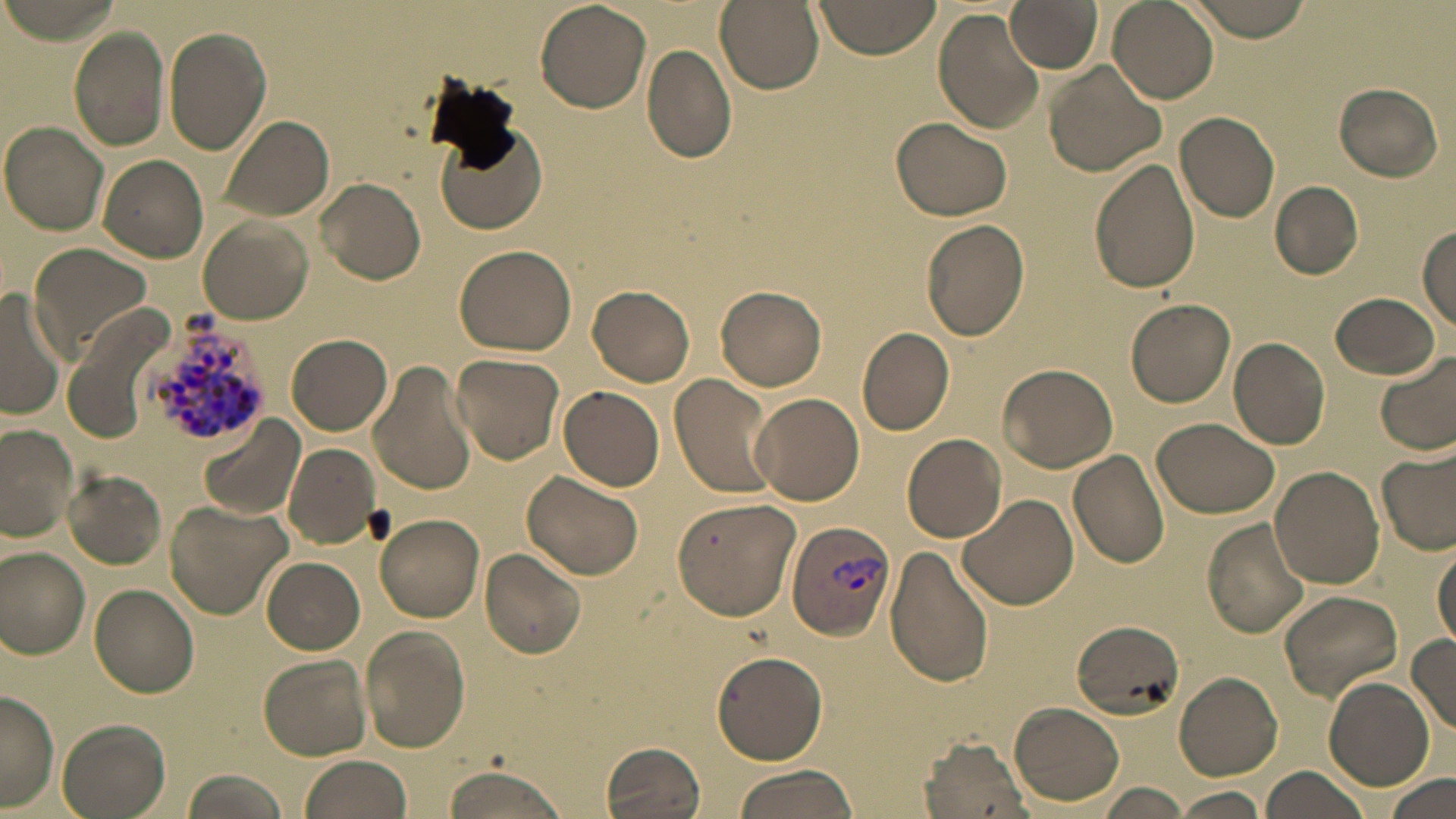
Approximate bounding boxes as (x1,y1)-(x2,y2) corner pairs in pixels. Plasmodium vivax-infected red blood cell locations: (140,313)-(276,451), (785,519)-(897,643). Uninfected red blood cell locations: (534,0)-(649,113), (715,0)-(823,93), (814,0)-(942,58), (1006,0)-(1103,72), (1107,0)-(1218,105), (1181,0)-(1316,41), (933,9)-(1045,134), (164,26)-(271,154), (69,28)-(169,151), (640,44)-(738,164), (1044,62)-(1165,179), (1334,82)-(1443,180), (1175,111)-(1279,221), (224,115)-(333,221), (891,116)-(1012,221), (1,122)-(111,235), (434,122)-(548,237), (100,154)-(208,261), (1088,158)-(1201,294), (316,177)-(425,286), (1270,181)-(1364,279), (920,217)-(1031,341), (200,218)-(313,324), (1417,227)-(1456,326), (30,242)-(154,364), (453,244)-(577,356), (589,285)-(695,387), (714,286)-(827,390), (0,292)-(66,421), (1330,292)-(1441,381), (1127,298)-(1235,406), (857,326)-(955,436), (287,333)-(391,435), (1228,337)-(1331,450), (451,353)-(565,466), (1375,353)-(1456,456), (368,360)-(479,497), (997,363)-(1118,473), (670,374)-(780,501), (558,386)-(665,491), (751,392)-(865,507), (196,416)-(304,522), (1153,417)-(1278,519), (0,424)-(78,544), (903,433)-(1007,542), (284,442)-(380,549), (1375,446)-(1456,558), (1068,448)-(1171,569), (1270,465)-(1384,588), (63,468)-(167,569), (520,471)-(644,581), (958,493)-(1078,611), (671,496)-(802,622), (165,500)-(290,620), (375,513)-(485,622), (1201,517)-(1313,638), (1433,541)-(1456,650), (884,544)-(995,689), (0,547)-(92,658), (480,547)-(586,659), (264,558)-(365,653), (90,583)-(201,697), (1278,590)-(1402,699), (1069,619)-(1188,720), (362,625)-(469,753), (1406,635)-(1456,735), (711,651)-(829,766), (259,654)-(372,760), (1174,671)-(1283,780), (1323,677)-(1433,789), (1,692)-(59,808), (1009,702)-(1126,806), (56,718)-(171,819), (919,734)-(1031,817), (602,741)-(709,819), (298,755)-(412,819), (436,764)-(569,819), (1261,765)-(1373,819), (728,766)-(859,819), (182,768)-(289,819), (1381,773)-(1454,817), (1096,784)-(1192,818), (1169,788)-(1270,818). Slide-level diagnosis: Plasmodium vivax. May-Grünwald-Giemsa stain. Thin blood film. 1000x magnification. Optical microscopy. Image is 1456×819 pixels. One field of a larger specimen.